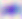 Captured at 400x magnification. Photomicrograph. Toxoplasma gondii is shown.